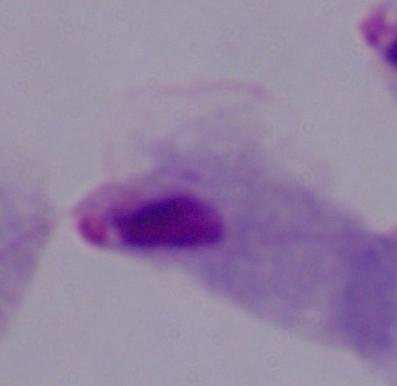

Summary:
  - Modality: micrograph
  - Identification: trichomonad
  - Magnification: 1000x